State which parasite is depicted.
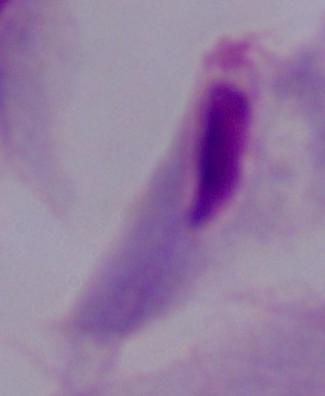
A trichomonad.

magnification: 1000x
modality: micrograph